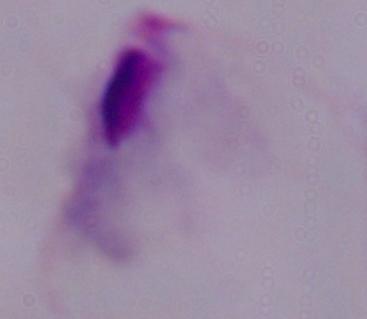
modality: micrograph
identification: trichomonad
magnification: 1000x